Assess the morphology of the red blood cells.
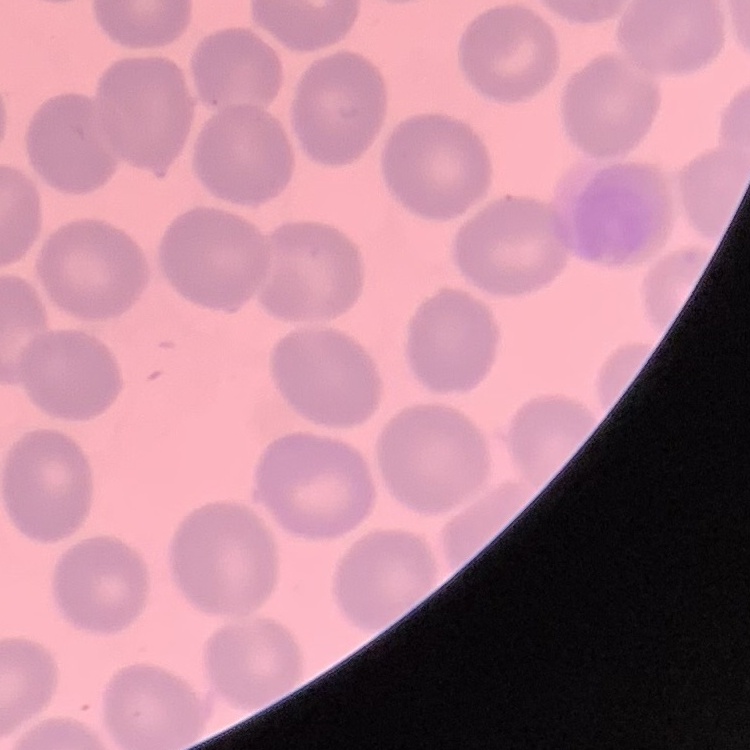

They show no rouleaux formation.

stain = Field's or Giemsa
preparation = thin peripheral smear
image type = square crop of a larger photomicrograph